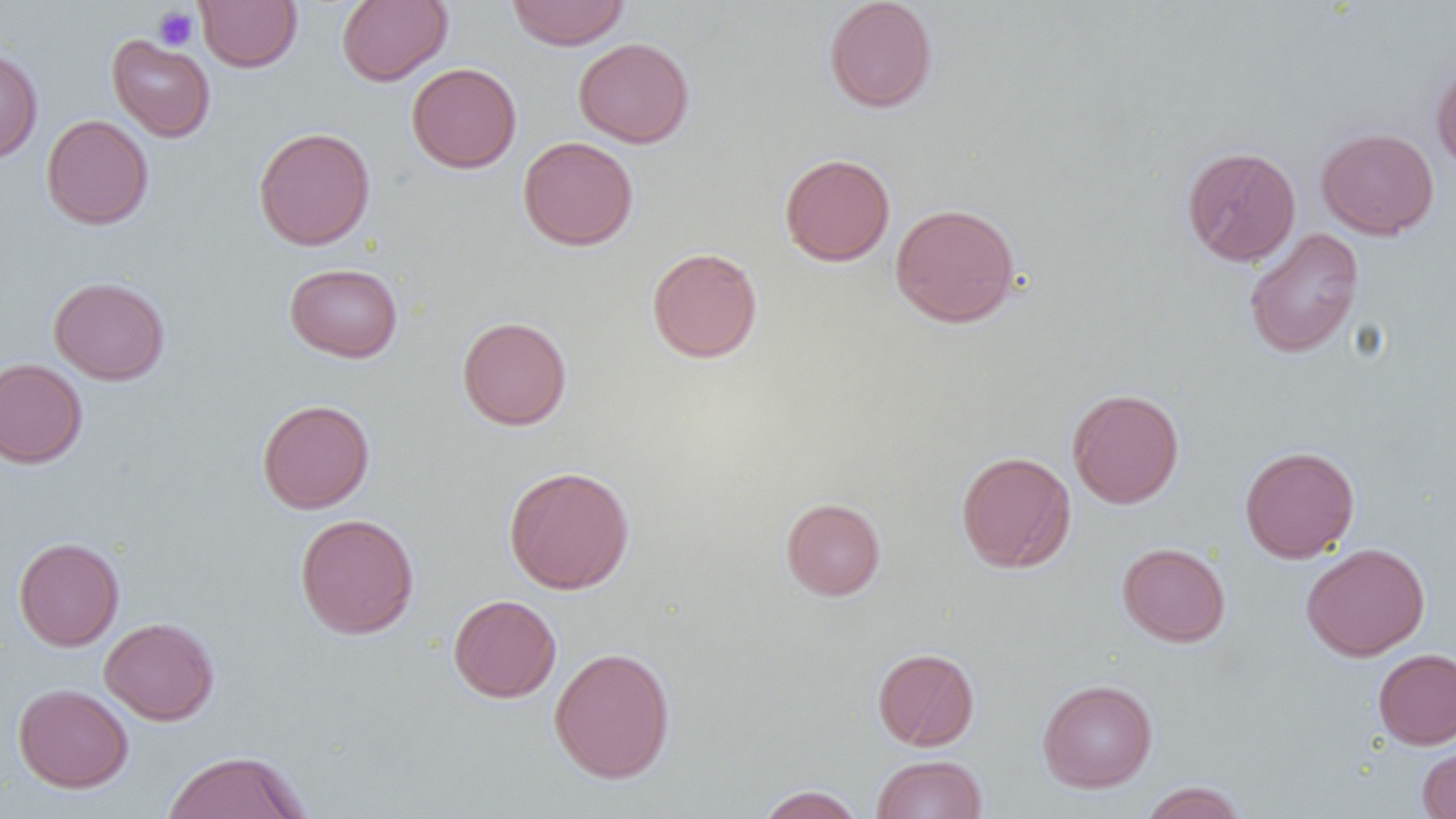
slide_level_diagnosis: no evidence of blood parasites
preparation: thin blood film
field_of_view: single
uninfected_red_blood_cell_locations: 'approximate bounding boxes as named x1/y1/x2/y2 corners in pixels: (x1=195, y1=0, x2=302, y2=72), (x1=337, y1=0, x2=452, y2=86), (x1=506, y1=0, x2=631, y2=50), (x1=823, y1=0, x2=938, y2=113), (x1=107, y1=34, x2=216, y2=142), (x1=573, y1=37, x2=694, y2=148), (x1=0, y1=46, x2=43, y2=164), (x1=1431, y1=60, x2=1456, y2=174), (x1=407, y1=63, x2=521, y2=173), (x1=41, y1=114, x2=154, y2=230), (x1=253, y1=127, x2=375, y2=251), (x1=1316, y1=127, x2=1439, y2=240), (x1=518, y1=136, x2=639, y2=251), (x1=1182, y1=146, x2=1301, y2=266), (x1=779, y1=153, x2=895, y2=266), (x1=890, y1=203, x2=1020, y2=327), (x1=1243, y1=228, x2=1364, y2=359), (x1=646, y1=247, x2=763, y2=363), (x1=283, y1=262, x2=403, y2=363), (x1=49, y1=276, x2=170, y2=385), (x1=457, y1=316, x2=572, y2=430), (x1=0, y1=358, x2=88, y2=469), (x1=1067, y1=387, x2=1184, y2=509), (x1=257, y1=399, x2=375, y2=514), (x1=1240, y1=445, x2=1360, y2=563), (x1=955, y1=451, x2=1076, y2=573), (x1=503, y1=465, x2=635, y2=595), (x1=780, y1=497, x2=886, y2=601), (x1=294, y1=513, x2=420, y2=639), (x1=13, y1=536, x2=124, y2=651), (x1=1117, y1=542, x2=1230, y2=647), (x1=1301, y1=542, x2=1430, y2=661), (x1=448, y1=594, x2=561, y2=703), (x1=99, y1=617, x2=219, y2=725), (x1=549, y1=646, x2=676, y2=784), (x1=872, y1=647, x2=980, y2=751), (x1=1373, y1=648, x2=1456, y2=749), (x1=1036, y1=679, x2=1157, y2=792), (x1=13, y1=683, x2=134, y2=793), (x1=1417, y1=744, x2=1456, y2=818), (x1=161, y1=749, x2=312, y2=818), (x1=871, y1=754, x2=988, y2=819), (x1=1139, y1=781, x2=1248, y2=819), (x1=755, y1=784, x2=866, y2=819)'
modality: optical microscopy
magnification: 1000x
image_size: 1456×819 pixels
platelet_locations: 'approximate bounding boxes as named x1/y1/x2/y2 corners in pixels: (x1=152, y1=6, x2=199, y2=51)'